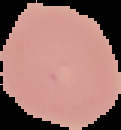
Summary:
  - Result: no malaria parasites seen
  - Preparation: thin blood film
  - Image size: 121×130 pixels
  - Image type: cell region segmented out of the field of view; surrounding area masked to black